Point out each leukocyte.
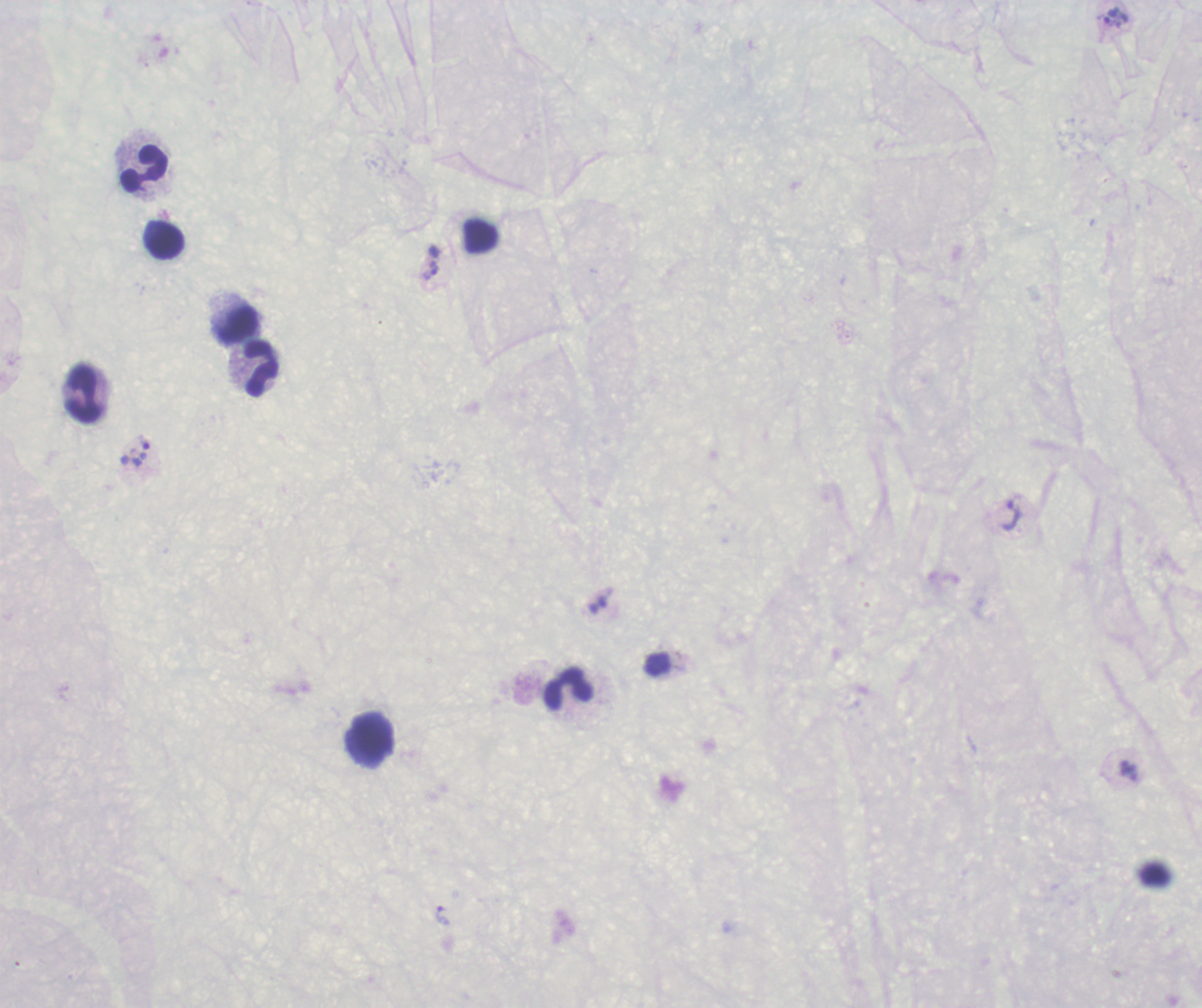

Approximate object centers, in pixels from the top-left corner.
Leukocytes: (x=145, y=169), (x=166, y=242), (x=239, y=326), (x=260, y=367), (x=83, y=395), (x=568, y=689).

Approximate object centers, in pixels from the top-left corner. Trophozoite locations: (x=1115, y=17), (x=431, y=271), (x=142, y=452), (x=1011, y=515), (x=442, y=915). Background quality: poor. Romanowsky stain. Result: positive for Plasmodium parasites. Image is 1202×1008 pixels. Coloration quality: bad. 100x magnification. Previously used in an actual diagnosis. One field from this slide. Thick blood film.